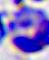
Summary:
  - Modality: micrograph
  - Magnification: 400x
  - Identification: leukocyte